Locate every Plasmodium falciparum-infected red blood cell.
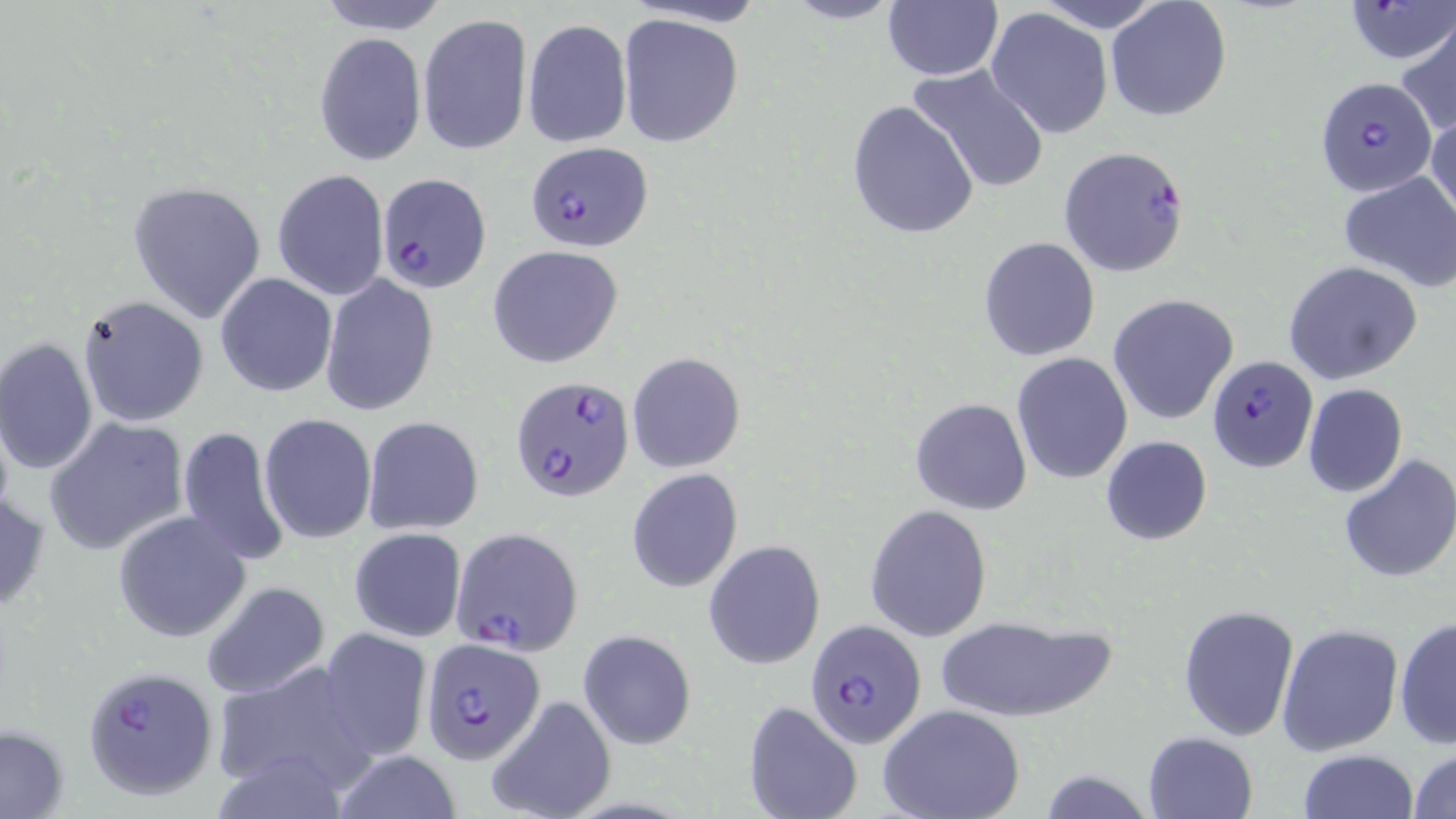
Approximate bounding boxes as [x1, y1, x2, y2] in pixels.
Plasmodium falciparum-infected red blood cells: [1316, 76, 1438, 198], [524, 141, 653, 251], [1057, 146, 1189, 278], [377, 173, 490, 294], [1208, 356, 1318, 472], [511, 375, 638, 503], [450, 526, 583, 654], [805, 620, 928, 750], [420, 641, 544, 763], [82, 665, 218, 800].

Summary:
  - Uninfected red blood cell locations: [313, 0, 454, 35], [625, 0, 770, 27], [779, 0, 906, 25], [881, 0, 1002, 81], [1039, 0, 1162, 31], [1105, 0, 1232, 122], [1345, 0, 1453, 64], [985, 6, 1113, 140], [418, 13, 533, 154], [618, 13, 745, 150], [521, 18, 632, 149], [1396, 18, 1456, 139], [312, 32, 427, 165], [906, 63, 1051, 195], [847, 100, 978, 241], [1427, 109, 1456, 228], [272, 170, 390, 302], [1339, 171, 1456, 293], [128, 180, 267, 324], [977, 237, 1100, 361], [487, 245, 623, 368], [1283, 261, 1424, 386], [215, 273, 338, 397], [321, 275, 438, 416], [1107, 294, 1239, 425], [75, 295, 209, 429], [0, 337, 100, 476], [1010, 352, 1133, 484], [627, 353, 745, 473], [1302, 382, 1408, 498], [910, 397, 1033, 515], [259, 413, 377, 543], [363, 415, 484, 535], [44, 417, 190, 555], [176, 425, 289, 567], [1101, 435, 1213, 545], [1338, 454, 1456, 583], [626, 468, 743, 592], [0, 484, 50, 619], [865, 503, 991, 640], [114, 511, 251, 643], [349, 526, 467, 642], [703, 539, 826, 669], [200, 581, 328, 700], [1177, 603, 1299, 742], [934, 613, 1115, 724], [1393, 618, 1455, 748], [1277, 623, 1403, 757], [318, 627, 432, 760], [578, 630, 696, 749], [209, 657, 379, 797], [486, 696, 616, 819], [743, 700, 863, 819], [880, 705, 1025, 819], [0, 725, 69, 819], [1142, 731, 1257, 819], [329, 748, 466, 819], [1298, 748, 1419, 819], [1408, 748, 1456, 819], [1038, 768, 1153, 819]
  - Slide-level diagnosis: Plasmodium falciparum
  - Field of view: one of a larger specimen
  - Preparation: thin blood smear
  - Image size: 1456×819 pixels
  - Magnification: 1000x
  - Stain: May-Grünwald-Giemsa
  - Modality: light microscopy